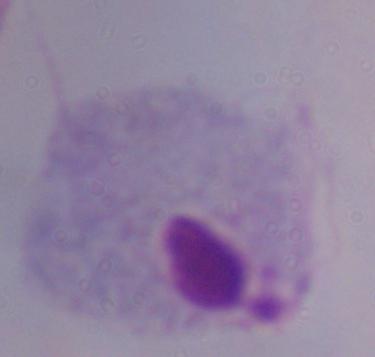

A trichomonad is shown. Micrograph. Captured at 1000x magnification.